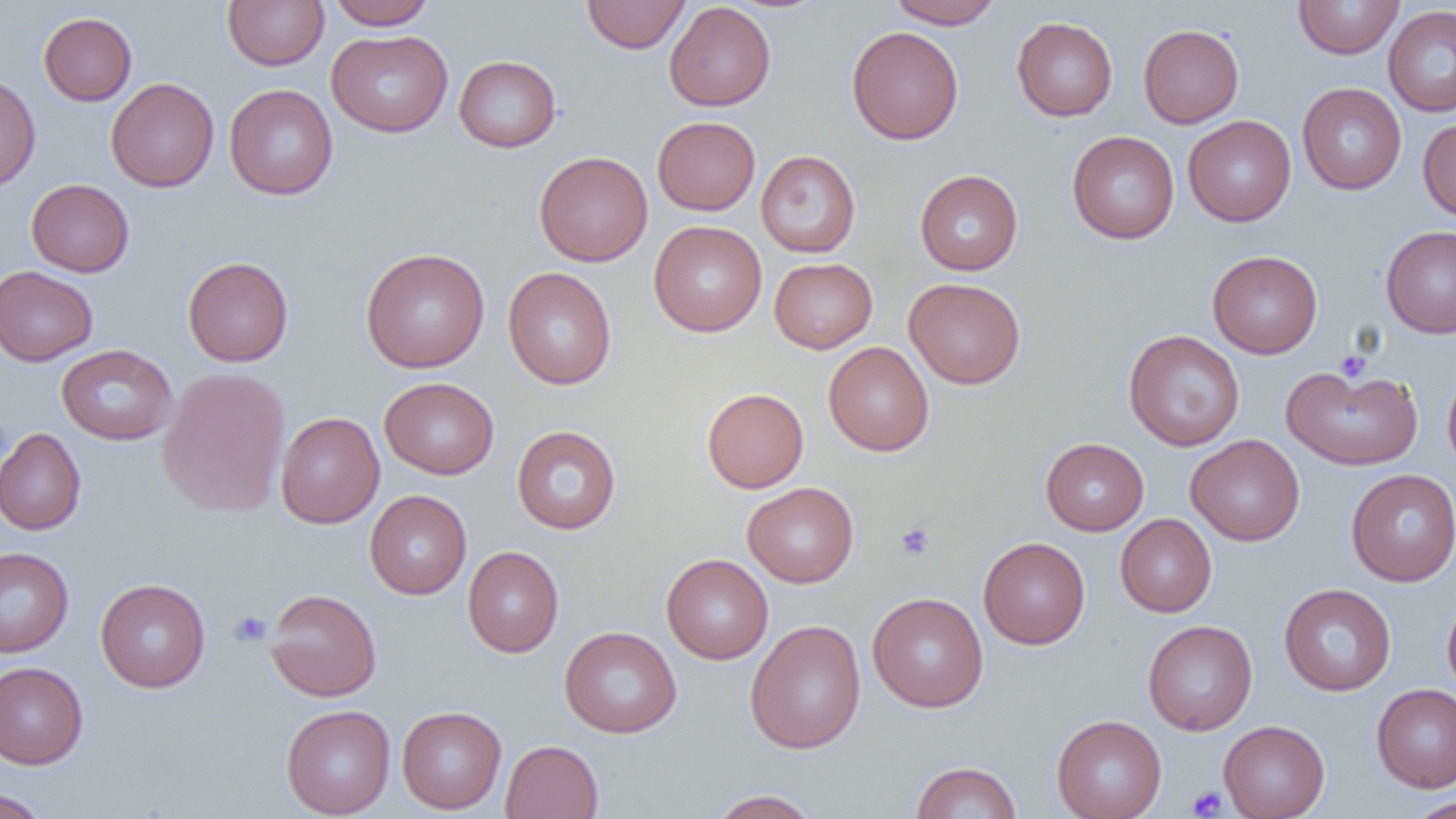
Summary:
  - Coordinate format: approximate bounding boxes as [x1, y1, x2, y2] in pixels
  - Platelet locations: [1335, 350, 1372, 383], [895, 521, 936, 560], [229, 611, 272, 647], [1186, 786, 1228, 818]
  - Uninfected red blood cell locations: [223, 0, 329, 70], [327, 0, 436, 30], [888, 0, 1003, 29], [1293, 0, 1404, 59], [581, 1, 690, 53], [664, 2, 776, 111], [1383, 5, 1456, 117], [38, 12, 137, 106], [1011, 17, 1118, 121], [1138, 23, 1244, 128], [846, 26, 963, 145], [326, 30, 453, 137], [454, 55, 561, 153], [0, 74, 40, 192], [106, 77, 219, 192], [1297, 83, 1407, 195], [224, 84, 338, 200], [1183, 115, 1296, 226], [652, 116, 760, 215], [1418, 117, 1456, 223], [1067, 131, 1179, 244], [756, 150, 860, 258], [534, 151, 653, 266], [915, 169, 1023, 275], [26, 179, 134, 277], [649, 220, 767, 337], [1381, 225, 1456, 338], [360, 247, 490, 373], [1208, 250, 1322, 358], [183, 256, 294, 367], [769, 258, 877, 353], [0, 265, 98, 366], [503, 267, 617, 390], [904, 277, 1025, 389], [1123, 330, 1245, 451], [823, 341, 934, 456], [56, 344, 177, 445], [1281, 362, 1423, 470], [1442, 365, 1456, 475], [157, 367, 290, 518], [380, 377, 499, 479], [702, 387, 809, 493], [275, 411, 384, 528], [512, 425, 622, 535], [0, 428, 86, 535], [1186, 435, 1305, 545], [1040, 438, 1149, 535], [1346, 469, 1456, 586], [742, 482, 859, 587], [365, 490, 471, 599], [1115, 514, 1216, 617], [978, 537, 1090, 649], [462, 546, 564, 657], [0, 547, 74, 658], [661, 553, 773, 664], [95, 578, 210, 692], [1279, 583, 1396, 696], [264, 588, 382, 701], [867, 591, 988, 712], [1442, 593, 1456, 701], [745, 619, 866, 754], [1142, 619, 1257, 735], [559, 626, 682, 738], [0, 662, 88, 768], [1371, 684, 1456, 791], [281, 704, 395, 818], [397, 706, 506, 814], [1051, 714, 1167, 819], [1218, 720, 1330, 819], [500, 740, 603, 818], [910, 761, 1022, 819], [0, 788, 53, 818], [706, 789, 823, 818], [1405, 796, 1456, 818]
  - Slide-level diagnosis: no evidence of blood parasites
  - Modality: light microscopy
  - Image size: 1456×819 pixels
  - Preparation: thin blood film
  - Magnification: 1000x
  - Field of view: one of a larger specimen